Classify this cell by malaria status.
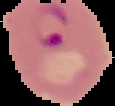

It is parasitized.

The area outside the segmented cell region is set to black. From a thin blood smear. Image is 115×106 pixels.